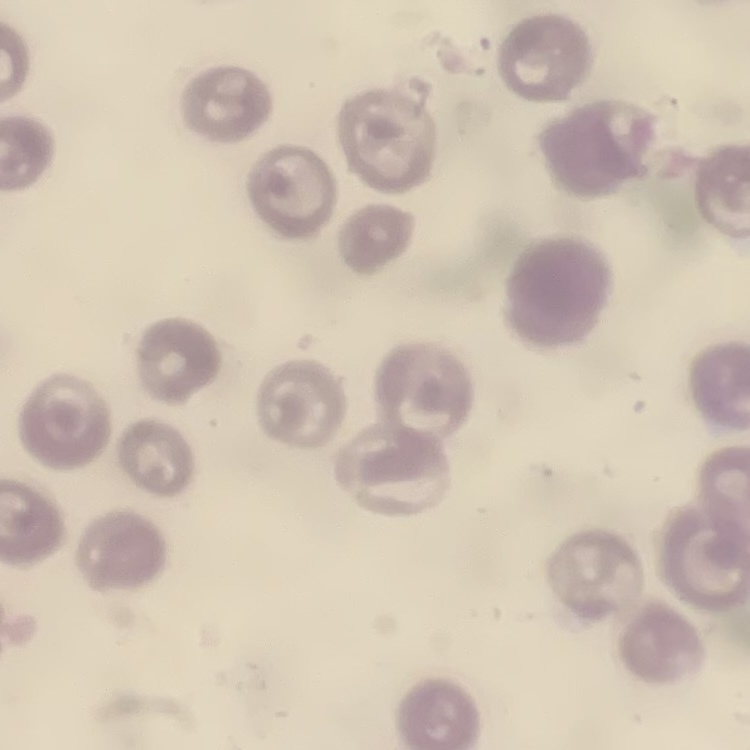

The red blood cells show no rouleaux formation. Stained with either Field's or Giemsa. One tile cut from a larger photomicrograph. Thin blood film.